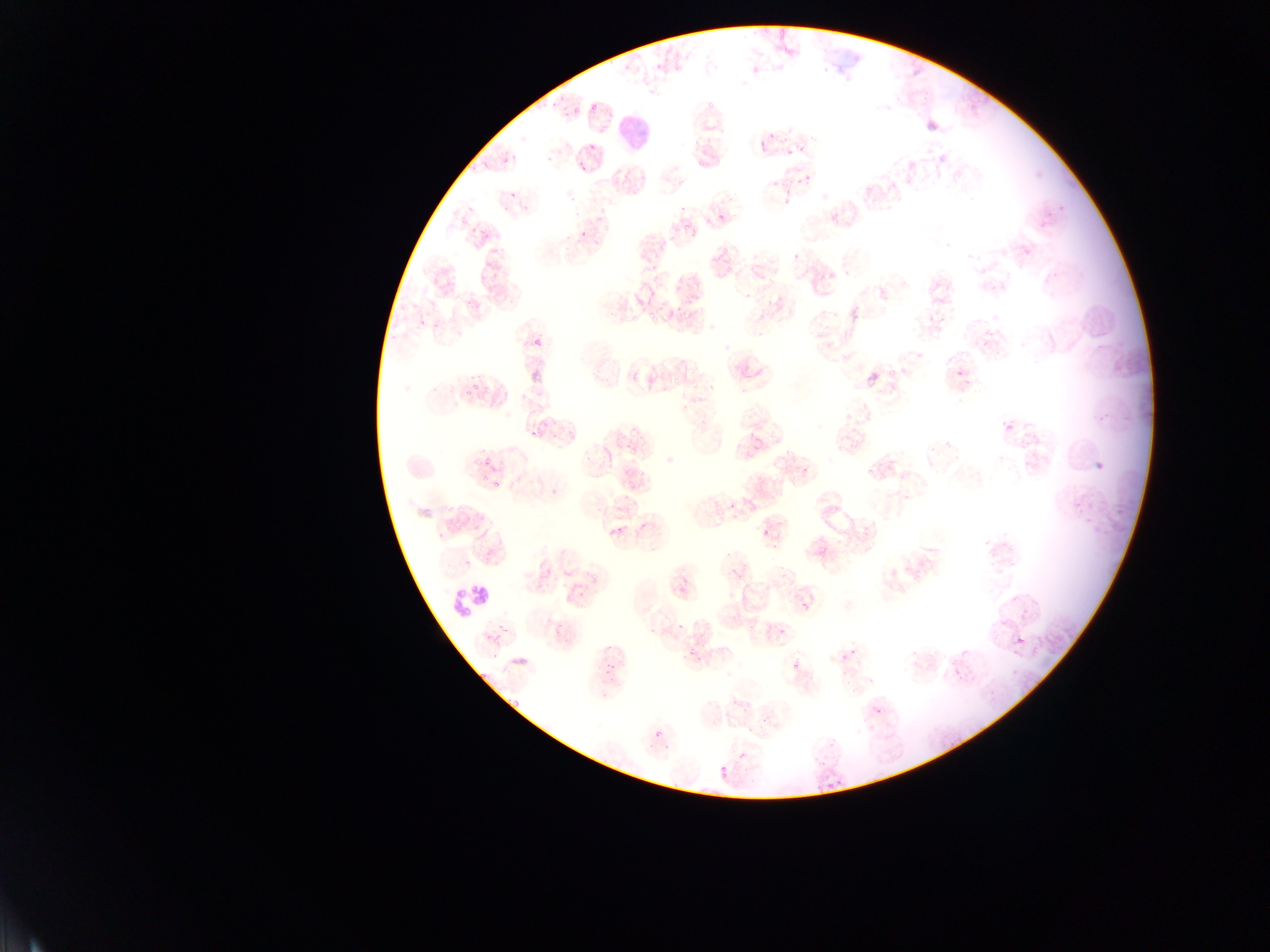 Approximate bounding boxes as [left, top, right, bottom] in pixels. Plasmodium parasite locations (subset; some below the resolvable size): [573, 106, 578, 114], [769, 131, 776, 140], [759, 139, 766, 147], [787, 149, 791, 157], [580, 165, 587, 174], [572, 194, 577, 205], [783, 200, 791, 206], [717, 215, 725, 221], [579, 231, 587, 237], [728, 268, 733, 277], [685, 310, 692, 319], [419, 319, 427, 326], [433, 323, 441, 328], [534, 336, 540, 345], [889, 366, 894, 376], [957, 367, 963, 376], [673, 376, 681, 384], [1008, 426, 1016, 429], [1088, 455, 1113, 474], [484, 457, 491, 466], [865, 468, 871, 476], [762, 532, 770, 537], [680, 621, 683, 630], [1018, 638, 1026, 644], [689, 651, 695, 659], [791, 663, 796, 671], [478, 669, 486, 677], [511, 701, 521, 709], [873, 704, 879, 713], [655, 731, 663, 736], [738, 752, 746, 757], [719, 765, 727, 778] | approximate [x, y] pixel centers of objects too small to bound: [594, 107], [592, 147], [505, 160], [808, 177], [789, 191], [512, 195], [683, 208], [795, 254], [653, 268], [761, 317], [654, 319], [670, 373], [475, 386], [468, 394], [533, 436], [805, 470], [486, 477], [497, 485], [466, 561], [684, 581], [681, 590], [500, 626], [781, 631], [651, 632], [498, 638], [609, 648], [853, 654], [495, 655], [843, 657], [608, 664], [607, 672], [611, 680], [604, 694]. Leukocyte locations: [619, 111, 648, 147], [452, 583, 489, 614]. Mobile-phone photograph taken through the microscope. Thin blood film. Image is 1270×952 pixels. One field of view. Collected in Ghana.